Identify the parasite.
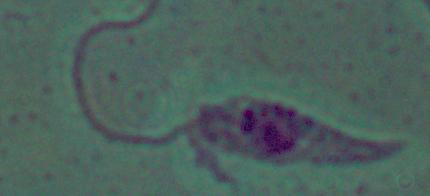
Leishmania.

Summary:
  - Modality: photomicrograph
  - Magnification: 1000x